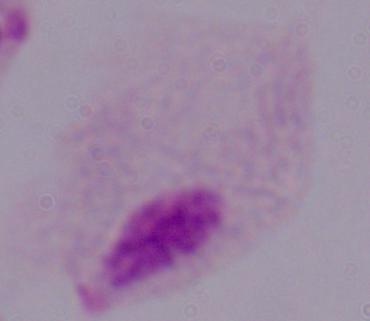

modality = photomicrograph
identification = trichomonad
magnification = 1000x